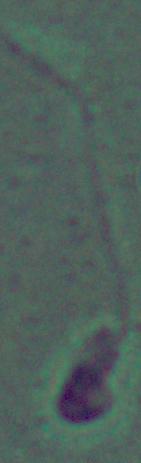

identification = Leishmania
modality = micrograph
magnification = 1000x